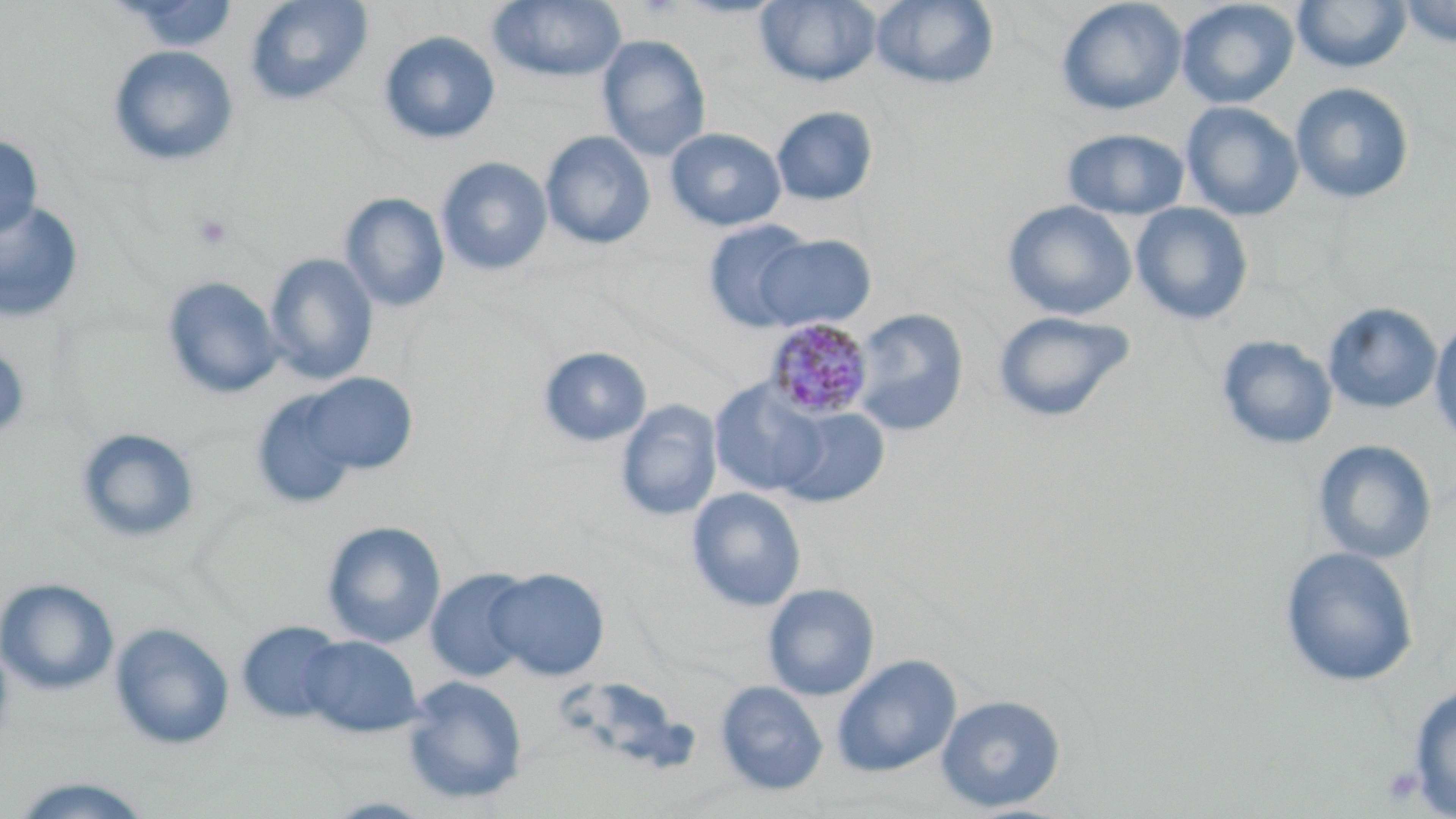

Approximate bounding boxes as named x1/y1/x2/y2 corners in pixels. Uninfected red blood cell locations: (x1=244, y1=0, x2=373, y2=106), (x1=488, y1=0, x2=628, y2=83), (x1=754, y1=0, x2=882, y2=88), (x1=870, y1=0, x2=1000, y2=90), (x1=1056, y1=0, x2=1188, y2=116), (x1=1176, y1=0, x2=1299, y2=109), (x1=1397, y1=0, x2=1456, y2=48), (x1=114, y1=1, x2=240, y2=52), (x1=1292, y1=1, x2=1413, y2=73), (x1=378, y1=30, x2=501, y2=145), (x1=597, y1=34, x2=711, y2=162), (x1=108, y1=44, x2=240, y2=168), (x1=1291, y1=82, x2=1414, y2=205), (x1=1181, y1=101, x2=1304, y2=221), (x1=770, y1=106, x2=878, y2=206), (x1=665, y1=127, x2=786, y2=232), (x1=1061, y1=128, x2=1190, y2=220), (x1=539, y1=130, x2=656, y2=251), (x1=0, y1=135, x2=43, y2=238), (x1=436, y1=156, x2=553, y2=277), (x1=339, y1=192, x2=450, y2=313), (x1=0, y1=200, x2=84, y2=323), (x1=1002, y1=200, x2=1137, y2=321), (x1=1131, y1=203, x2=1254, y2=325), (x1=702, y1=219, x2=815, y2=332), (x1=753, y1=234, x2=876, y2=332), (x1=264, y1=252, x2=379, y2=386), (x1=161, y1=276, x2=284, y2=399), (x1=1322, y1=302, x2=1443, y2=414), (x1=851, y1=309, x2=968, y2=437), (x1=991, y1=310, x2=1135, y2=423), (x1=1429, y1=314, x2=1456, y2=446), (x1=1216, y1=335, x2=1338, y2=450), (x1=0, y1=344, x2=31, y2=445), (x1=538, y1=346, x2=652, y2=448), (x1=300, y1=372, x2=418, y2=475), (x1=710, y1=380, x2=828, y2=496), (x1=250, y1=388, x2=361, y2=509), (x1=616, y1=400, x2=722, y2=521), (x1=776, y1=406, x2=890, y2=508), (x1=74, y1=427, x2=201, y2=545), (x1=1312, y1=439, x2=1436, y2=564), (x1=687, y1=487, x2=807, y2=612), (x1=321, y1=520, x2=446, y2=649), (x1=1279, y1=546, x2=1419, y2=688), (x1=487, y1=568, x2=609, y2=681), (x1=426, y1=569, x2=533, y2=682), (x1=0, y1=577, x2=119, y2=694), (x1=762, y1=583, x2=880, y2=700), (x1=236, y1=620, x2=347, y2=724), (x1=110, y1=622, x2=234, y2=749), (x1=299, y1=634, x2=422, y2=738), (x1=0, y1=636, x2=15, y2=756), (x1=831, y1=654, x2=962, y2=777), (x1=715, y1=674, x2=957, y2=791), (x1=401, y1=676, x2=528, y2=805), (x1=715, y1=680, x2=828, y2=796), (x1=1407, y1=683, x2=1456, y2=818), (x1=935, y1=694, x2=1066, y2=813), (x1=6, y1=776, x2=159, y2=818). Plasmodium malariae-infected red blood cell locations: (x1=765, y1=319, x2=873, y2=421). Platelet locations: (x1=191, y1=211, x2=235, y2=252), (x1=1381, y1=765, x2=1426, y2=806). Slide-level diagnosis: Plasmodium malariae. 1000x magnification. Image is 1456×819 pixels. Single field of view. May-Grünwald-Giemsa-stained preparation. Optical microscopy. Thin blood smear.